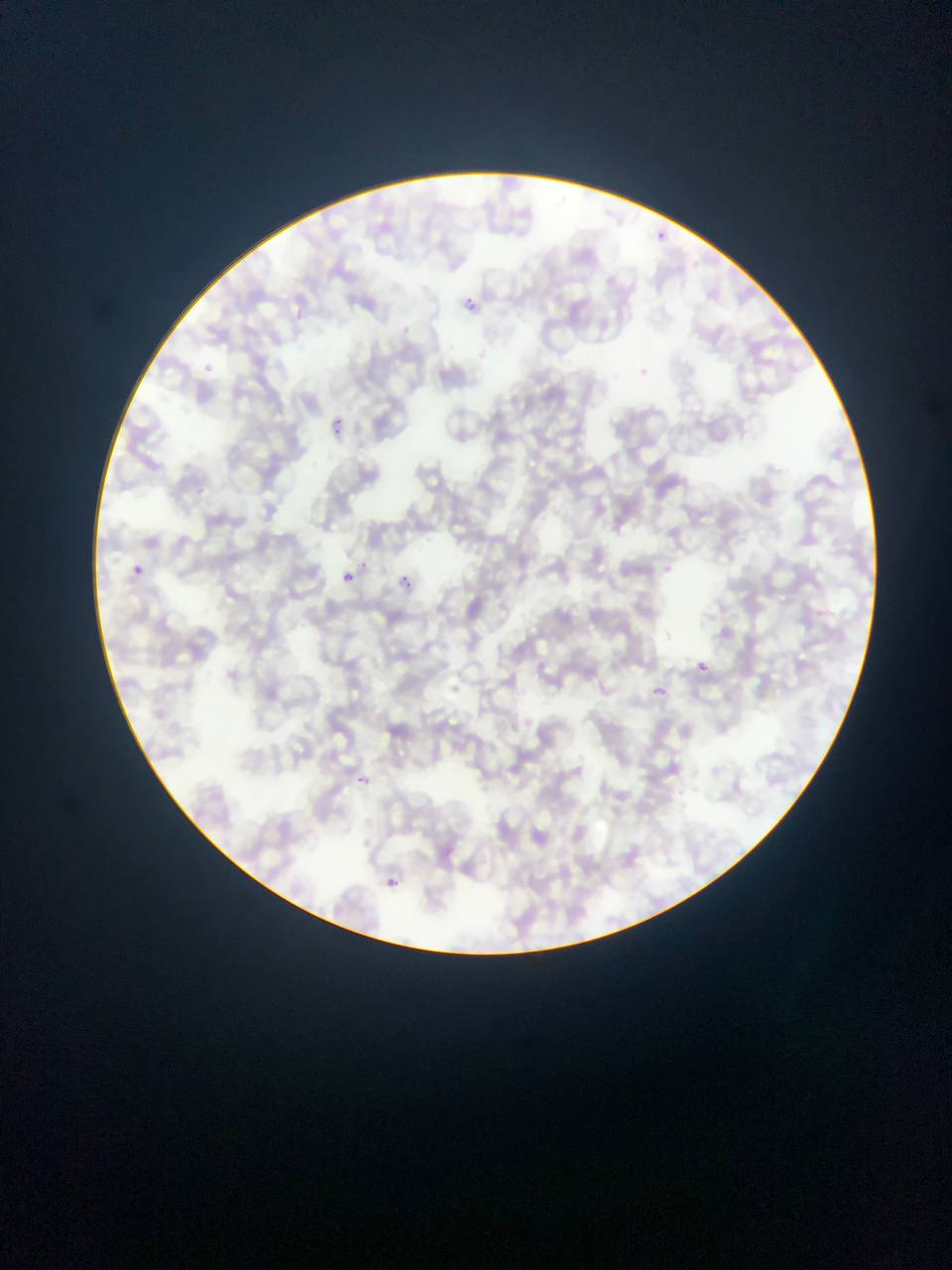
Approximate bounding boxes as (left, top, right, bottom) in pixels. Plasmodium parasite locations: (657, 220, 677, 253), (460, 292, 501, 309), (197, 361, 223, 379), (326, 410, 345, 435), (355, 556, 374, 577), (132, 564, 144, 576), (343, 570, 354, 582), (399, 576, 424, 610), (686, 652, 713, 675), (649, 678, 673, 695), (347, 763, 379, 795), (384, 871, 414, 888). Mobile-phone photograph taken through the microscope. Image is 952×1270 pixels. Single field of view. Sample from Ghana. Thin blood film.